Assess this cell for malaria.
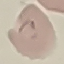

Parasitized.

{
  "preparation": "thin blood film",
  "image_type": "automatically extracted cell patch, resized to 64 × 64 pixels",
  "stain": "Giemsa",
  "capture": "smartphone through the microscope eyepiece"
}